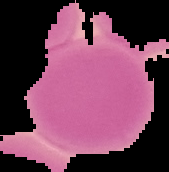

{
  "image_size": "169×172 pixels",
  "malaria_status": "uninfected",
  "image_type": "cell region segmented out of the field of view; surrounding area masked to black",
  "preparation": "thin blood film"
}